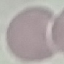
Result: no malaria parasites seen. Automatically extracted cell patch, resized to 64 × 64 pixels. Giemsa-stained preparation. Thin blood film. Acquired by smartphone through the microscope eyepiece.